Name the cell type shown.
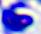

A leukocyte.

modality = micrograph
magnification = 400x